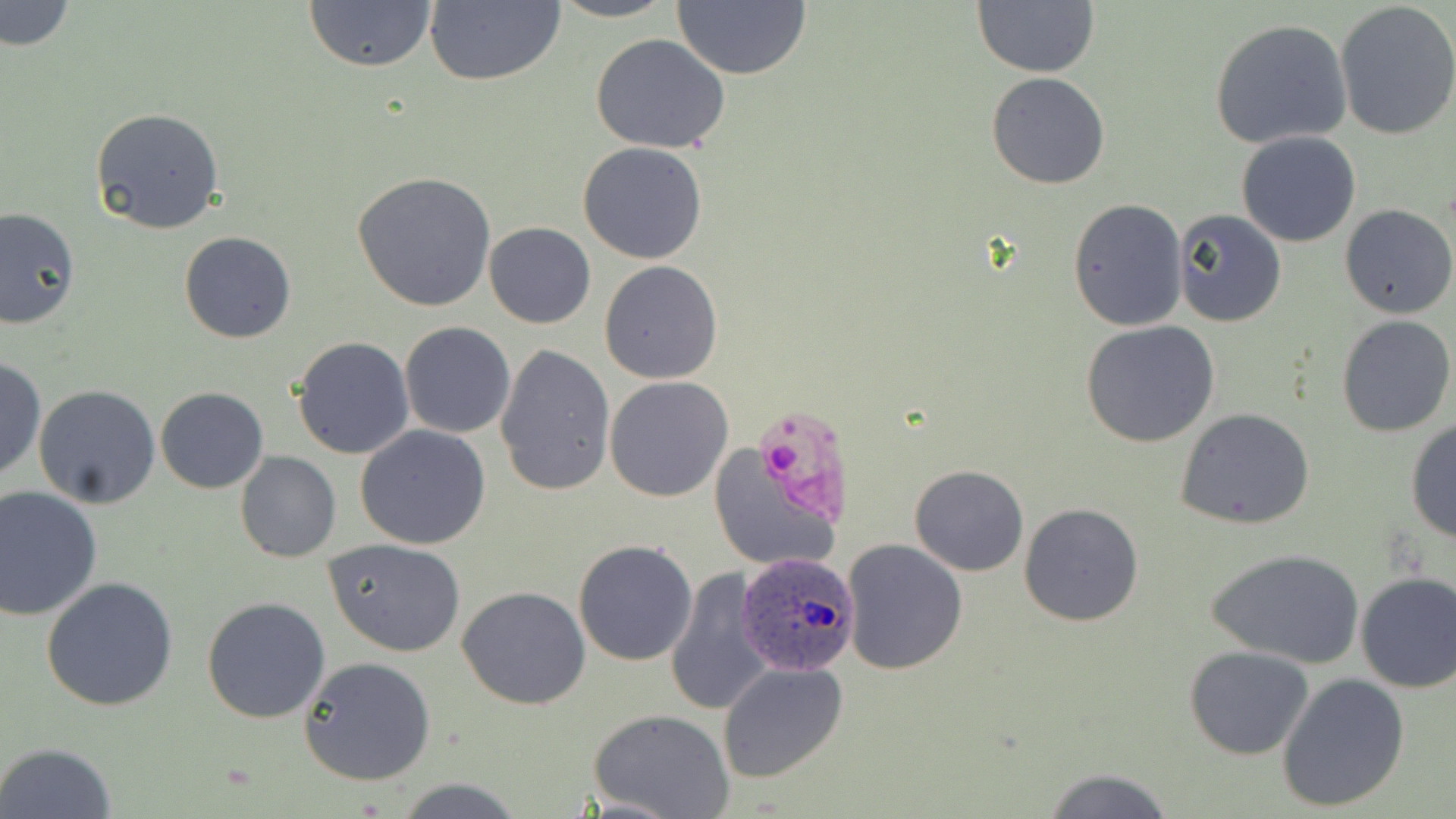
slide-level diagnosis = Plasmodium ovale
image size = 1456×819 pixels
Plasmodium ovale-infected red blood cell locations = approximate bounding boxes as (x1, y1, x2, y2) in pixels: (735, 552, 860, 678)
uninfected red blood cell locations = approximate bounding boxes as (x1, y1, x2, y2) in pixels: (1, 0, 74, 52), (302, 0, 438, 73), (547, 0, 679, 23), (424, 1, 566, 87), (671, 1, 811, 80), (972, 1, 1100, 78), (1333, 2, 1456, 142), (1208, 18, 1355, 151), (589, 35, 733, 154), (987, 72, 1110, 190), (89, 106, 226, 234), (1236, 131, 1362, 247), (578, 143, 709, 264), (352, 171, 496, 311), (1068, 198, 1188, 330), (1340, 205, 1455, 318), (0, 207, 79, 330), (1172, 209, 1287, 328), (484, 221, 596, 329), (179, 231, 297, 343), (599, 261, 722, 384), (1336, 315, 1455, 438), (1080, 320, 1221, 448), (399, 322, 516, 438), (292, 336, 414, 459), (495, 343, 617, 496), (0, 356, 45, 482), (604, 377, 733, 503), (32, 384, 162, 509), (155, 387, 268, 494), (1176, 408, 1317, 531), (1404, 418, 1456, 543), (355, 425, 492, 550), (706, 443, 843, 573), (235, 451, 341, 562), (909, 465, 1029, 576), (0, 487, 102, 620), (1018, 503, 1143, 627), (325, 538, 467, 656), (841, 538, 968, 674), (572, 539, 699, 667), (1207, 548, 1365, 668), (662, 568, 772, 717), (1354, 571, 1456, 693), (41, 577, 178, 711), (458, 586, 590, 709), (202, 596, 331, 723), (1185, 646, 1314, 760), (299, 656, 436, 786), (718, 662, 850, 785), (1275, 672, 1409, 814), (590, 709, 734, 819), (2, 740, 117, 818), (1040, 766, 1176, 819), (396, 778, 524, 817)
stain = May-Grünwald-Giemsa
field of view = single
magnification = 1000x
preparation = thin blood film
modality = light microscopy